Comment on the morphology of the red blood cells.
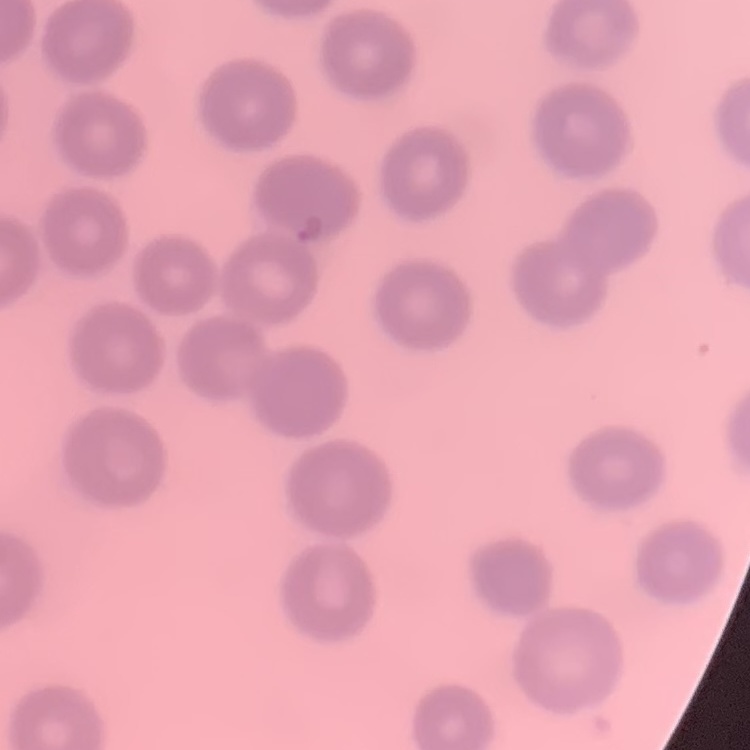

No rouleaux formation.

Stained with either Field's or Giemsa. Thin blood film. One tile cut from a larger photomicrograph.